Describe the morphology of the erythrocytes.
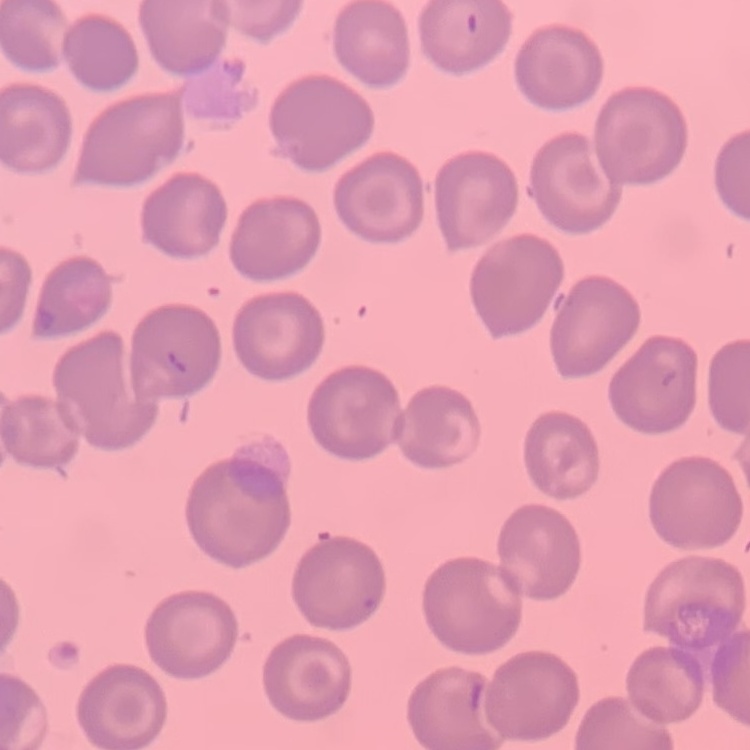

They show no rouleaux formation.

stain = Field's or Giemsa
preparation = thin blood film
image type = one tile cut from a larger photomicrograph